Classify this cell by malaria status.
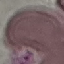

Uninfected.

Summary:
  - Capture: smartphone through the microscope eyepiece
  - Stain: Giemsa
  - Image type: cell patch, automatically extracted from a larger field of view and resized to 64 × 64 pixels
  - Preparation: thin blood film